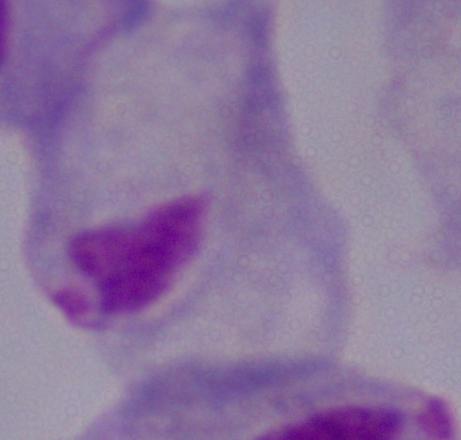
identification = trichomonad
magnification = 1000x
modality = photomicrograph